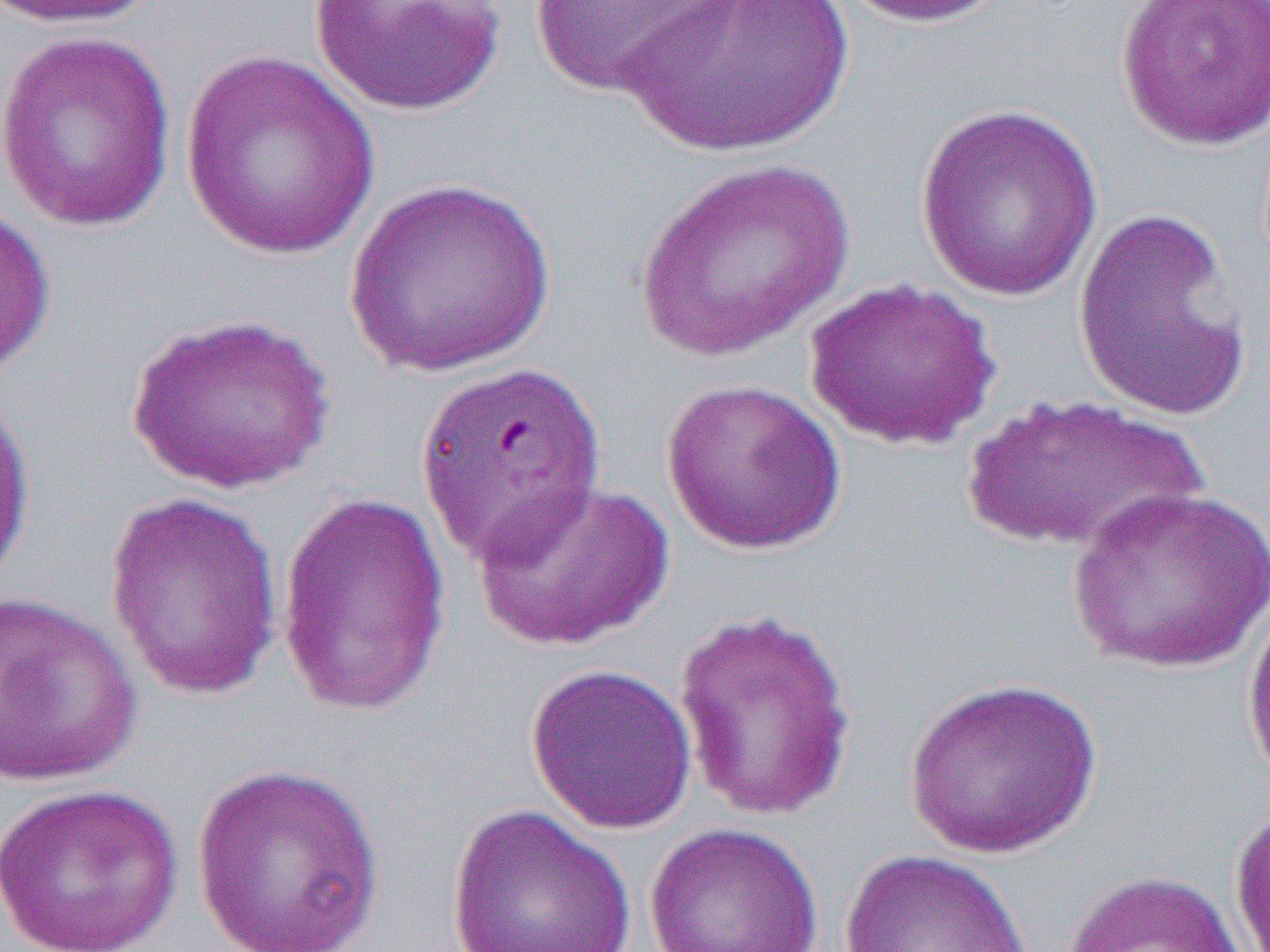

Summary:
  - Coordinate format: approximate bounding boxes as named x1/y1/x2/y2 corners in pixels
  - Uninfected red blood cell locations: (x1=5, y1=0, x2=164, y2=29), (x1=309, y1=0, x2=508, y2=117), (x1=623, y1=0, x2=854, y2=157), (x1=839, y1=0, x2=1014, y2=28), (x1=1114, y1=0, x2=1269, y2=151), (x1=526, y1=1, x2=737, y2=98), (x1=0, y1=28, x2=178, y2=234), (x1=179, y1=50, x2=382, y2=261), (x1=915, y1=103, x2=1103, y2=301), (x1=632, y1=158, x2=856, y2=363), (x1=343, y1=178, x2=558, y2=380), (x1=0, y1=203, x2=56, y2=384), (x1=1072, y1=207, x2=1254, y2=421), (x1=804, y1=278, x2=1001, y2=451), (x1=124, y1=311, x2=337, y2=495), (x1=413, y1=358, x2=610, y2=567), (x1=660, y1=378, x2=847, y2=556), (x1=0, y1=385, x2=37, y2=602), (x1=959, y1=391, x2=1210, y2=555), (x1=470, y1=479, x2=675, y2=652), (x1=1066, y1=484, x2=1268, y2=675), (x1=104, y1=491, x2=285, y2=701), (x1=276, y1=491, x2=452, y2=719), (x1=1240, y1=580, x2=1270, y2=798), (x1=0, y1=589, x2=144, y2=789), (x1=672, y1=607, x2=860, y2=824), (x1=525, y1=663, x2=698, y2=835), (x1=904, y1=677, x2=1102, y2=860), (x1=191, y1=761, x2=388, y2=952), (x1=0, y1=782, x2=186, y2=952), (x1=1230, y1=799, x2=1270, y2=951), (x1=446, y1=804, x2=638, y2=952), (x1=643, y1=822, x2=825, y2=952), (x1=837, y1=848, x2=1034, y2=952), (x1=1061, y1=869, x2=1246, y2=952)
  - Slide-level diagnosis: Plasmodium falciparum
  - Image size: 1270×952 pixels
  - Modality: optical microscopy
  - Preparation: thin blood film
  - Field of view: one of a larger specimen
  - Magnification: 1000x